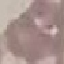

result = no malaria parasites seen
image type = automatically extracted cell patch, resized to 64 × 64 pixels
preparation = thin smear
stain = Giemsa
capture = smartphone through the microscope eyepiece